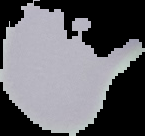

Summary:
  - Image size: 145×136 pixels
  - Image type: segmented cell region on a black background
  - Preparation: thin blood smear
  - Malaria status: uninfected